Report the malaria status of this cell.
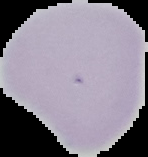

Uninfected.

Summary:
  - Image type: cell region segmented out of the field of view; surrounding area masked to black
  - Preparation: thin blood smear
  - Image size: 148×157 pixels